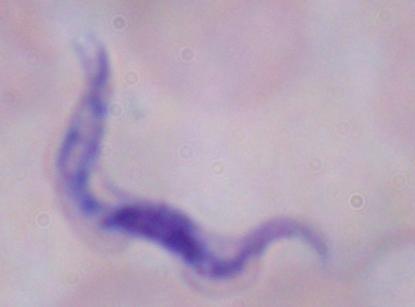 A trypanosome is seen. 1000x magnification. Micrograph.